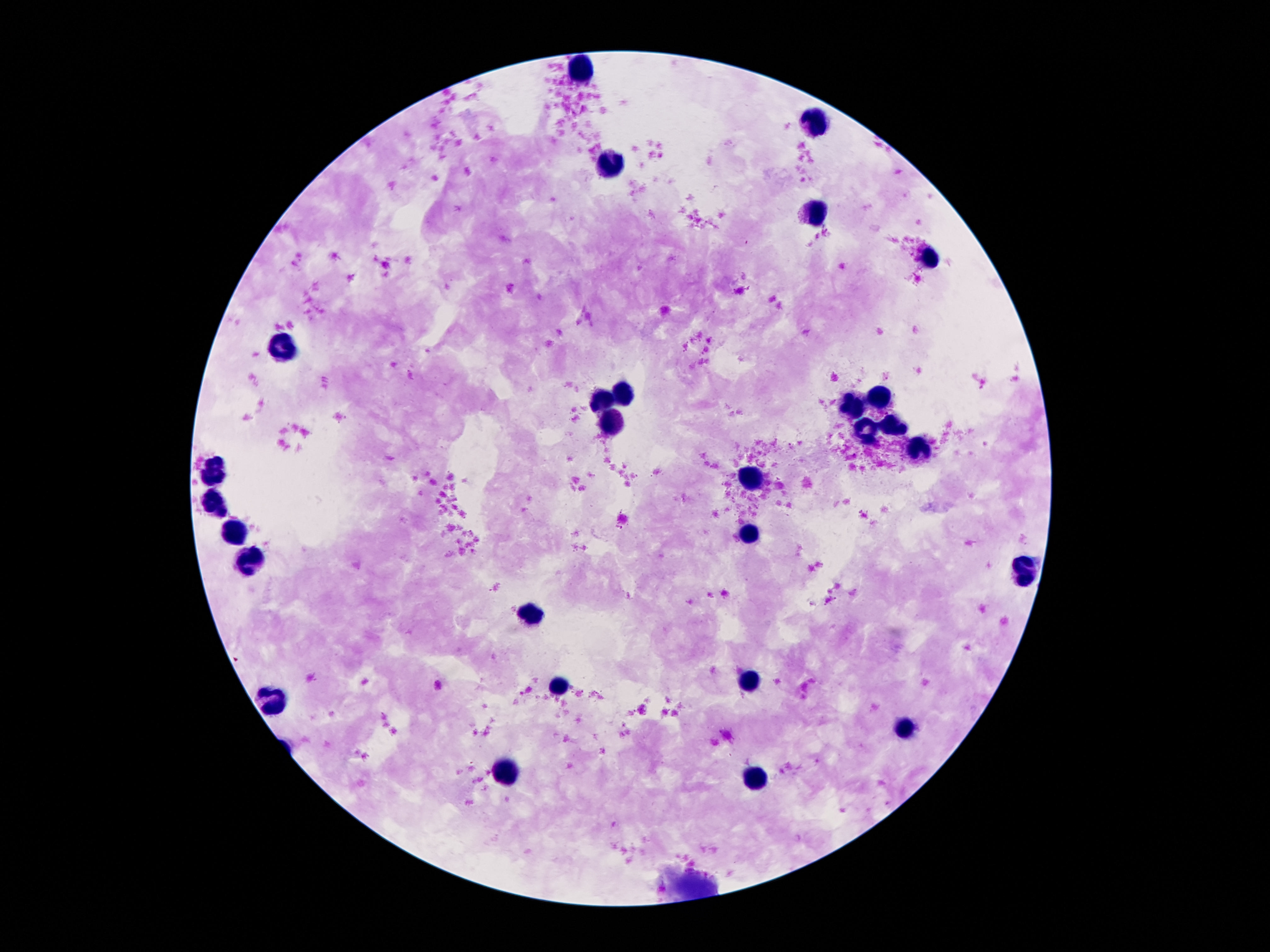

Approximate centers as [x, y] in pixels.
Summary:
  - Leukocyte locations: [585, 67], [820, 122], [614, 162], [812, 214], [930, 256], [285, 351], [626, 389], [884, 394], [606, 399], [856, 404], [616, 424], [894, 427], [866, 429], [922, 450], [217, 474], [752, 478], [219, 504], [235, 533], [748, 534], [253, 556], [1024, 572], [532, 612], [752, 680], [562, 684], [275, 698], [904, 730], [508, 769], [760, 781]
  - Capture: smartphone camera through the microscope eyepiece
  - Magnification: 100x
  - Patient malaria status: negative
  - Image size: 1270×952 pixels
  - Preparation: thick peripheral-blood smear
  - Field of view: single
  - Stain: Giemsa